Name the parasite shown.
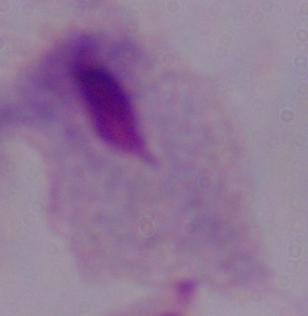

A trichomonad.

Summary:
  - Modality: photomicrograph
  - Magnification: 1000x